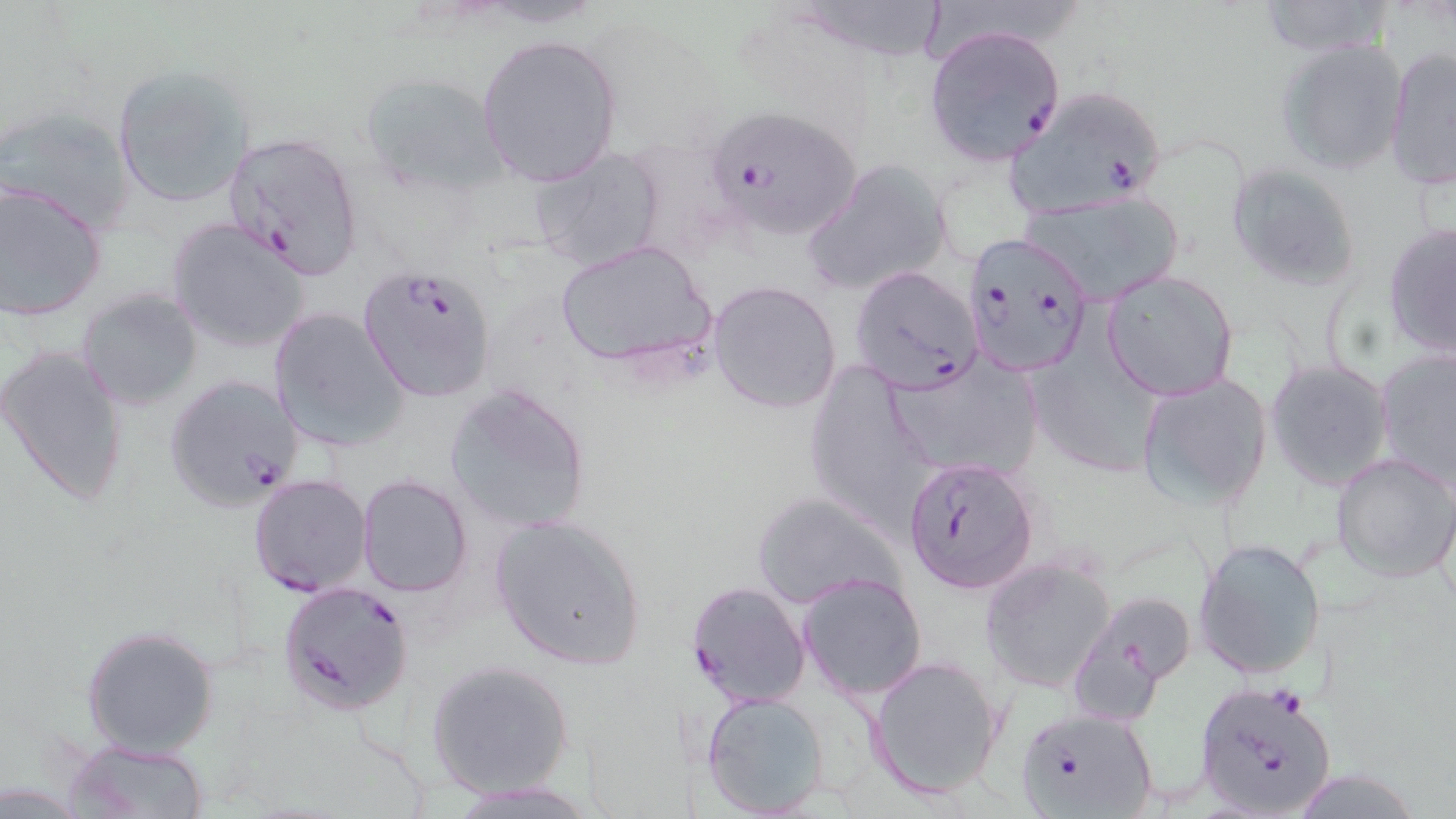
Summary:
  - Coordinate format: approximate bounding boxes as (x1,y1)-(x2,y2) corner pairs in pixels
  - Uninfected red blood cell locations: (784,0)-(947,65), (1254,0)-(1398,58), (477,33)-(623,188), (1274,37)-(1409,176), (1383,49)-(1455,191), (111,65)-(257,208), (359,69)-(508,193), (0,106)-(135,233), (530,145)-(669,270), (803,160)-(954,293), (1226,162)-(1361,291), (0,184)-(108,322), (1020,190)-(1185,303), (166,217)-(313,355), (1384,224)-(1456,358), (555,240)-(713,374), (1102,269)-(1239,401), (708,279)-(841,414), (76,288)-(202,411), (267,306)-(408,452), (1036,324)-(1154,479), (1,343)-(131,508), (1377,352)-(1456,486), (884,358)-(1042,483), (1266,359)-(1394,490), (803,362)-(936,528), (1137,372)-(1273,509), (444,382)-(593,533), (1331,451)-(1456,581), (357,474)-(474,598), (752,491)-(905,612), (488,513)-(648,672), (1194,537)-(1327,681), (980,555)-(1118,693), (798,572)-(927,702), (1073,589)-(1198,710), (81,623)-(220,758), (867,655)-(1006,800), (426,659)-(574,797), (700,691)-(832,818), (65,738)-(212,818), (449,778)-(597,816)
  - Plasmodium falciparum-infected red blood cell locations: (923,25)-(1065,166), (1007,83)-(1171,218), (708,106)-(863,238), (222,128)-(367,279), (972,236)-(1094,373), (357,263)-(498,402), (849,264)-(986,395), (162,374)-(305,512), (904,455)-(1040,595), (249,474)-(373,597), (278,579)-(414,717), (686,580)-(811,708), (1193,678)-(1338,819), (1014,707)-(1159,819)
  - Slide-level diagnosis: Plasmodium falciparum
  - Preparation: thin blood film
  - Modality: light microscopy
  - Image size: 1456×819 pixels
  - Field of view: one of a larger specimen
  - Stain: May-Grünwald-Giemsa
  - Magnification: 1000x